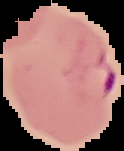

Summary:
  - Preparation: thin blood smear
  - Malaria status: parasitized
  - Image size: 124×151 pixels
  - Image type: segmented cell region on a black background